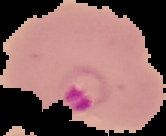
Summary:
  - Result: Plasmodium parasites detected
  - Preparation: thin blood smear
  - Image type: segmented cell region with the area outside set to black
  - Image size: 166×136 pixels